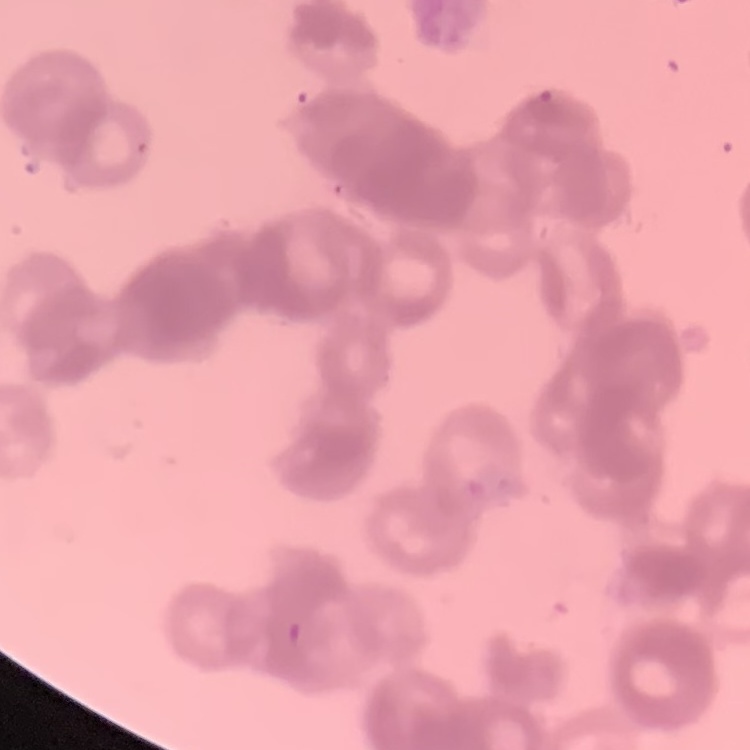
The red blood cells show rouleaux formation. One tile cut from a larger photomicrograph. Thin blood smear. Stained with either Field's or Giemsa.